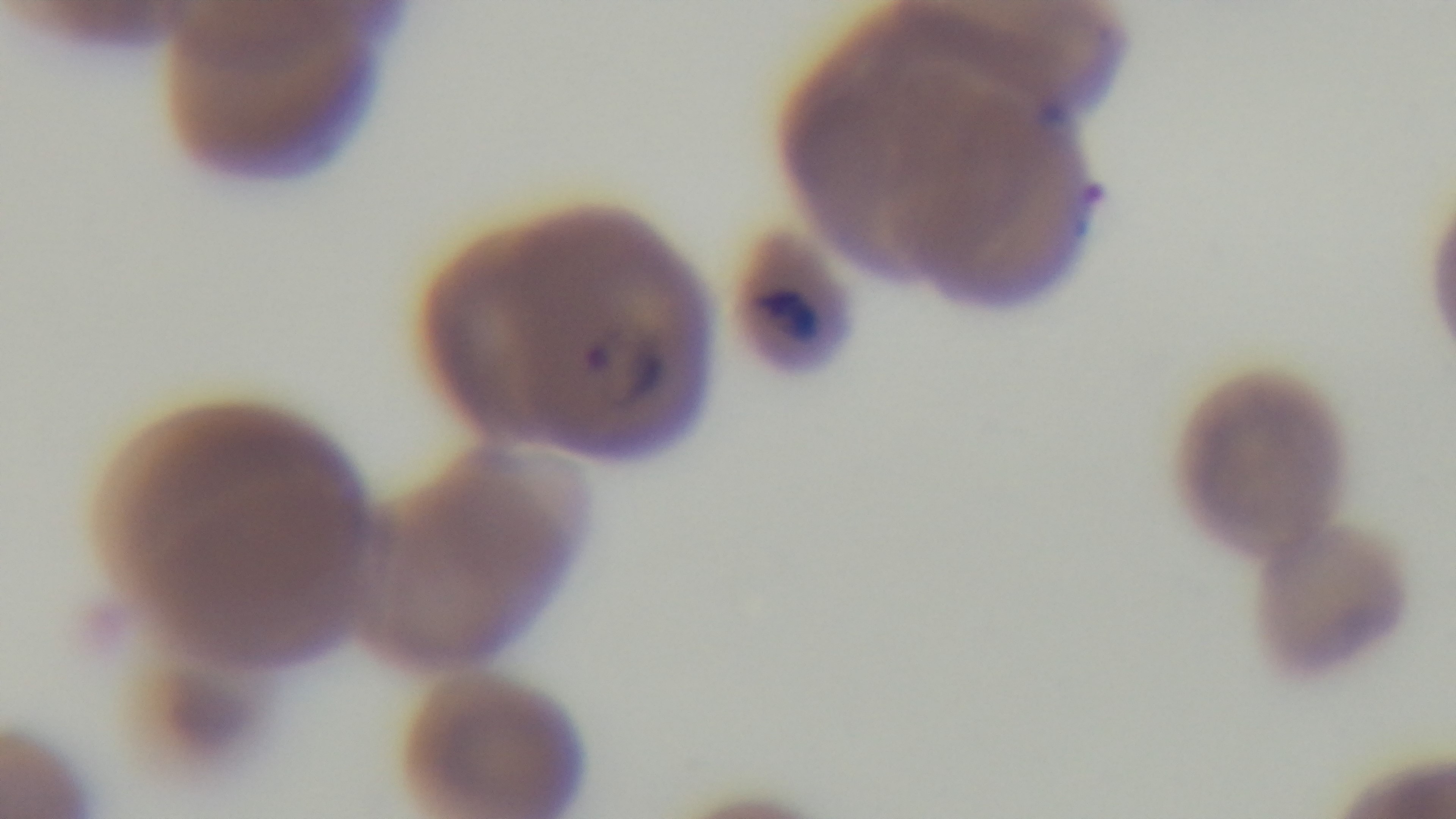

field of view = single
objective = 100x oil immersion
stain = Giemsa
modality = light microscopy
preparation = thin
malaria status = infected
capture = mounted 4K digital camera